Outline each Plasmodium ovale-infected red blood cell.
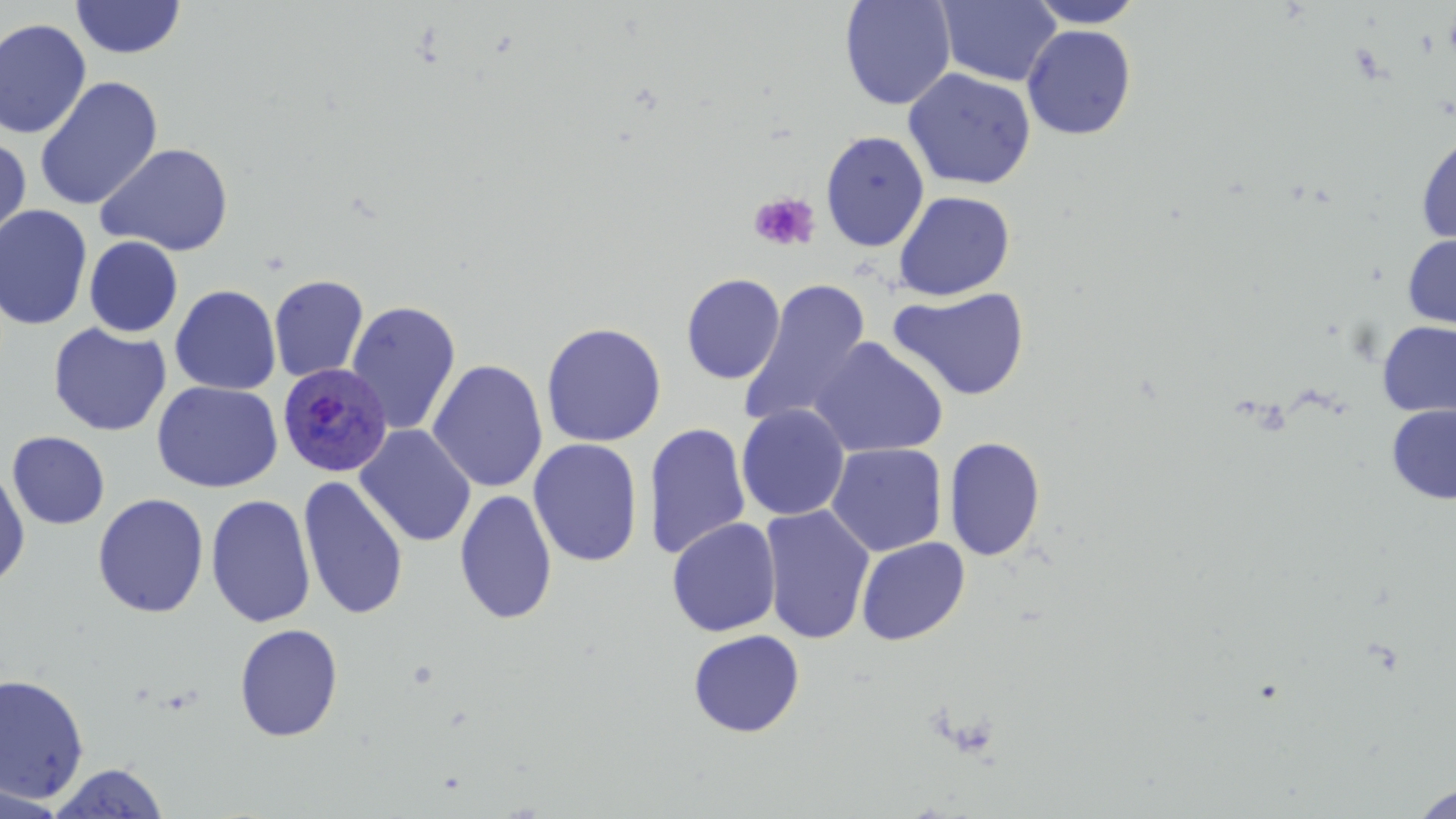

Approximate bounding boxes as (x1,y1)-(x2,y2) corner pairs in pixels.
Plasmodium ovale-infected red blood cells: (277,362)-(394,478).

Summary:
  - Platelet locations: (750,192)-(820,252)
  - Uninfected red blood cell locations: (70,0)-(186,59), (839,0)-(956,110), (936,0)-(1062,87), (1026,0)-(1146,28), (0,18)-(92,139), (1022,25)-(1137,140), (903,69)-(1036,190), (34,76)-(163,211), (821,130)-(930,252), (1415,131)-(1456,247), (0,136)-(31,252), (95,142)-(234,257), (893,190)-(1015,301), (0,204)-(92,330), (1402,233)-(1456,331), (84,236)-(183,337), (681,273)-(785,384), (269,274)-(369,383), (740,279)-(872,430), (169,285)-(281,395), (889,286)-(1030,401), (345,300)-(462,436), (540,321)-(666,448), (1377,321)-(1456,417), (48,323)-(171,437), (809,337)-(948,458), (427,359)-(548,493), (152,380)-(284,493), (736,404)-(850,521), (1387,404)-(1456,504), (643,421)-(752,559), (355,424)-(476,548), (7,431)-(110,530), (943,436)-(1046,562), (528,438)-(643,567), (826,443)-(948,556), (0,465)-(30,590), (297,475)-(409,621), (454,488)-(557,626), (93,493)-(209,618), (205,493)-(316,628), (759,504)-(875,645), (666,518)-(782,637), (856,537)-(970,646), (234,623)-(344,742), (687,629)-(805,737), (0,672)-(90,804), (47,762)-(171,818), (0,782)-(70,818), (1411,783)-(1456,819)
  - Slide-level diagnosis: Plasmodium ovale
  - Image size: 1456×819 pixels
  - Magnification: 1000x
  - Preparation: thin blood film
  - Stain: May-Grünwald-Giemsa
  - Field of view: one of a larger specimen
  - Modality: light microscopy